Assess for Plasmodium parasites.
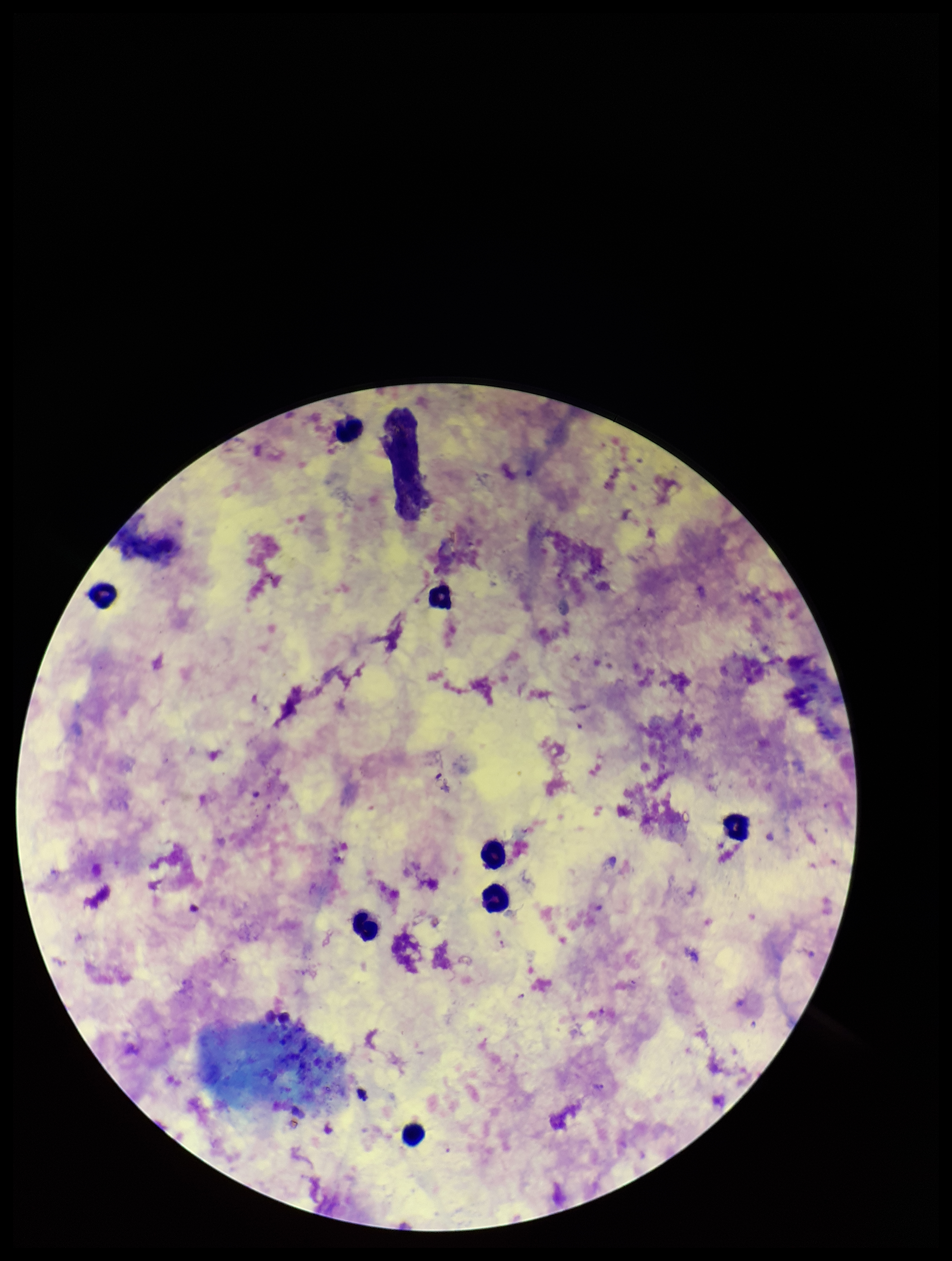

Detected.

Smartphone photograph taken through the eyepiece of a microscope. Patient malaria status: infected. Parasite count: 2. Leukocyte count: 8. Image is 952×1261 pixels. Preparation: thick. Stained with Giemsa. One field from this slide. Species reported for this patient: Plasmodium falciparum.